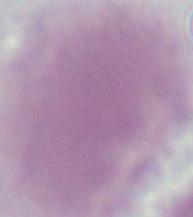

identification = red blood cell
modality = photomicrograph
magnification = 1000x